Report the malaria status.
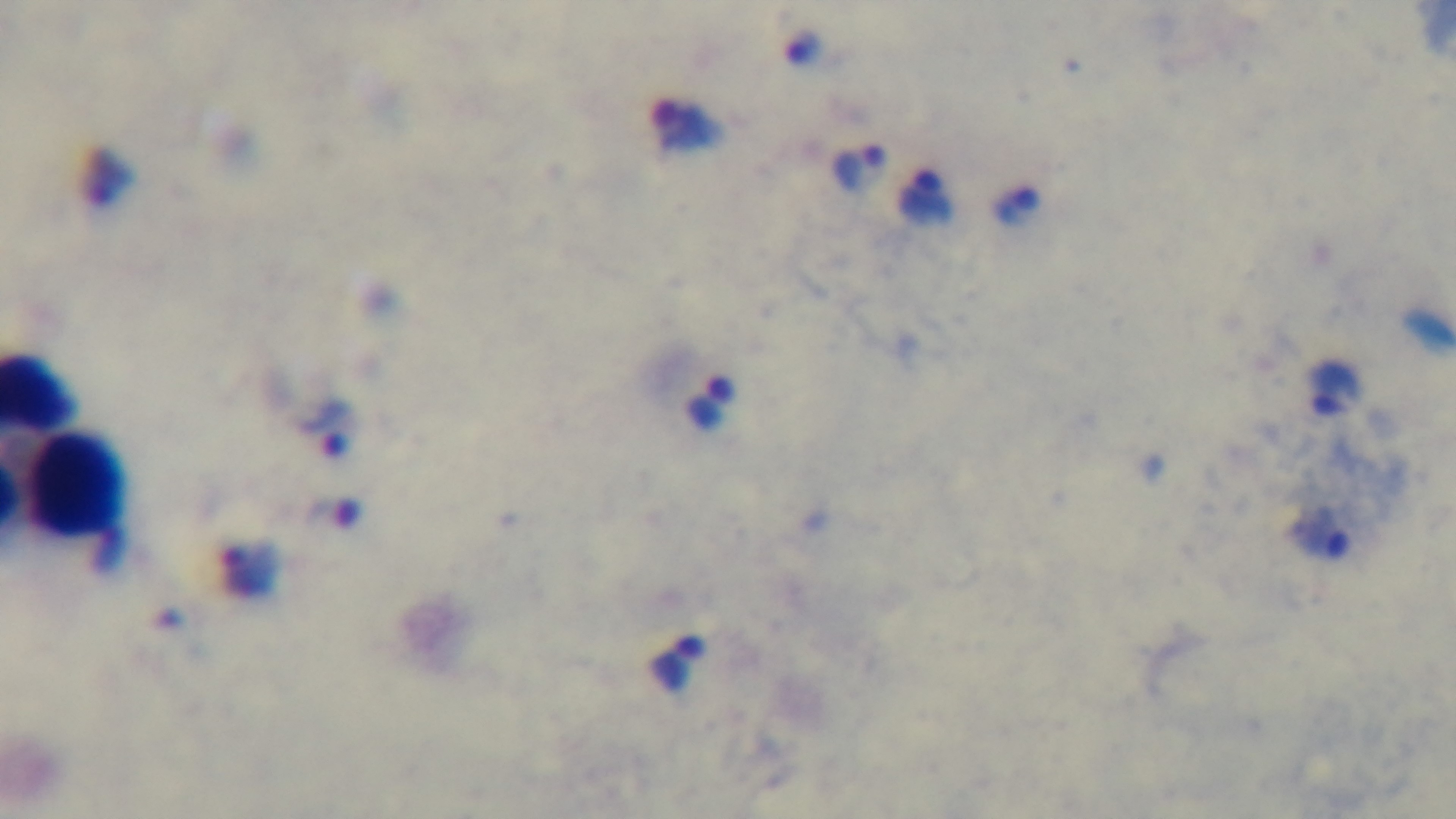
Positive.

Summary:
  - Capture: mounted 4K digital camera
  - Field of view: one from the slide
  - Stain: Giemsa
  - Objective: 100x oil immersion
  - Preparation: thick blood film
  - Modality: light microscopy